Outline platelets.
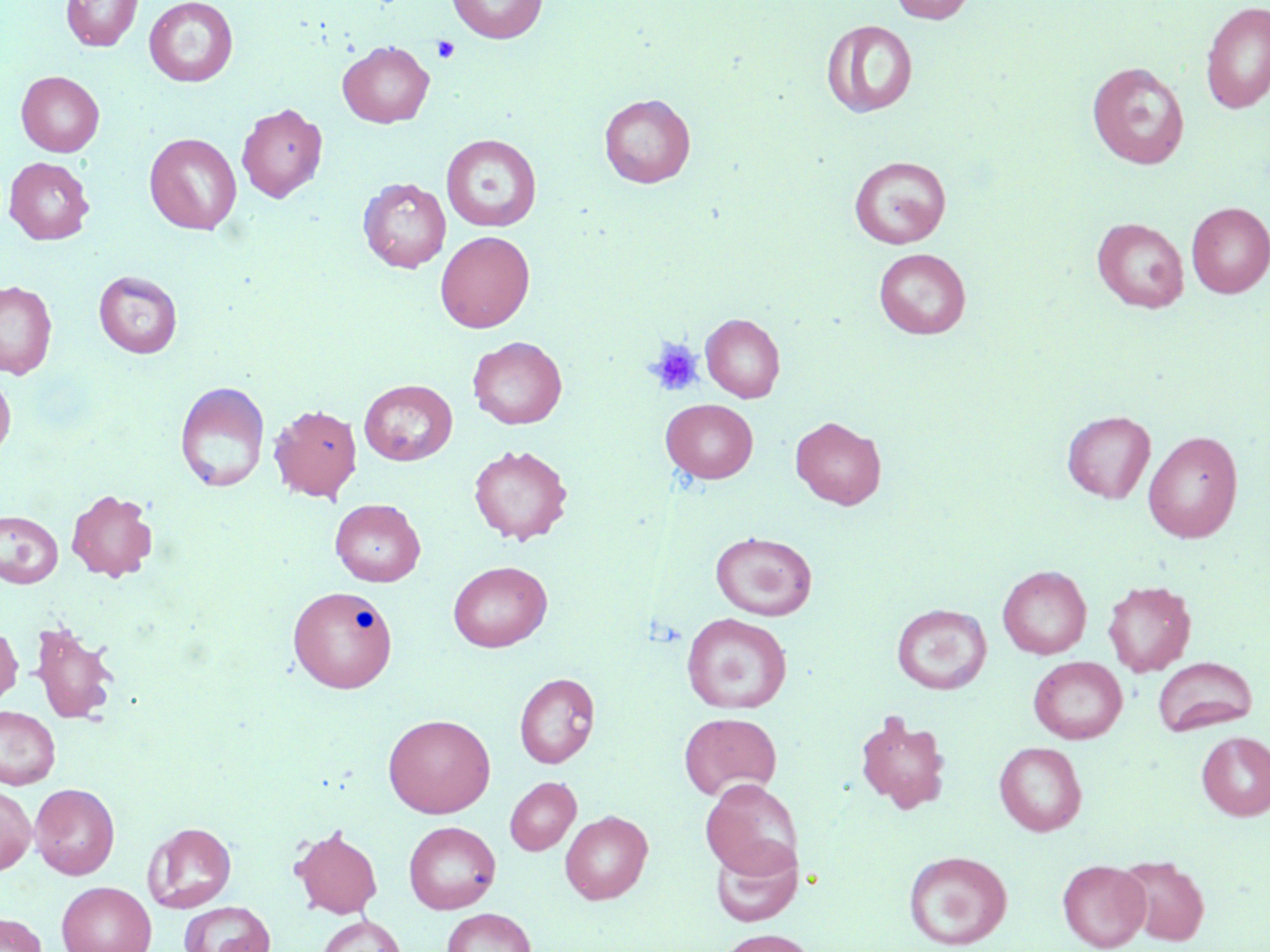

Approximate bounding boxes as named x1/y1/x2/y2 corners in pixels.
Platelets: (x1=432, y1=36, x2=460, y2=63), (x1=646, y1=338, x2=704, y2=396).

{
  "slide_level_diagnosis": "no evidence of blood parasites",
  "preparation": "thin blood film",
  "magnification": "1000x",
  "uninfected_red_blood_cell_locations": "approximate bounding boxes as named x1/y1/x2/y2 corners in pixels: (x1=60, y1=0, x2=143, y2=51), (x1=144, y1=0, x2=238, y2=87), (x1=446, y1=0, x2=547, y2=43), (x1=889, y1=0, x2=976, y2=24), (x1=1200, y1=2, x2=1270, y2=115), (x1=822, y1=20, x2=918, y2=118), (x1=338, y1=41, x2=434, y2=127), (x1=1087, y1=61, x2=1190, y2=169), (x1=16, y1=71, x2=104, y2=157), (x1=599, y1=94, x2=695, y2=188), (x1=237, y1=102, x2=327, y2=203), (x1=144, y1=132, x2=242, y2=234), (x1=441, y1=133, x2=542, y2=232), (x1=849, y1=156, x2=951, y2=249), (x1=4, y1=157, x2=94, y2=245), (x1=358, y1=177, x2=451, y2=273), (x1=1186, y1=202, x2=1270, y2=298), (x1=1092, y1=218, x2=1189, y2=313), (x1=435, y1=231, x2=534, y2=332), (x1=874, y1=248, x2=970, y2=339), (x1=94, y1=270, x2=183, y2=358), (x1=0, y1=280, x2=57, y2=379), (x1=701, y1=313, x2=785, y2=402), (x1=468, y1=336, x2=567, y2=429), (x1=0, y1=370, x2=15, y2=461), (x1=359, y1=379, x2=457, y2=466), (x1=175, y1=381, x2=270, y2=493), (x1=661, y1=399, x2=758, y2=483), (x1=269, y1=404, x2=362, y2=502), (x1=1062, y1=410, x2=1156, y2=503), (x1=791, y1=416, x2=886, y2=509), (x1=1143, y1=430, x2=1244, y2=543), (x1=469, y1=444, x2=573, y2=545), (x1=66, y1=489, x2=158, y2=581), (x1=330, y1=498, x2=425, y2=587), (x1=0, y1=511, x2=64, y2=588), (x1=711, y1=531, x2=817, y2=621), (x1=448, y1=561, x2=552, y2=652), (x1=998, y1=565, x2=1091, y2=659), (x1=1103, y1=580, x2=1196, y2=676), (x1=287, y1=586, x2=396, y2=692), (x1=891, y1=604, x2=992, y2=694), (x1=682, y1=613, x2=792, y2=714), (x1=29, y1=621, x2=120, y2=725), (x1=0, y1=623, x2=22, y2=707), (x1=1029, y1=656, x2=1127, y2=744), (x1=1153, y1=657, x2=1257, y2=736), (x1=514, y1=673, x2=600, y2=768), (x1=0, y1=706, x2=60, y2=789), (x1=853, y1=709, x2=952, y2=814), (x1=679, y1=712, x2=782, y2=800), (x1=383, y1=713, x2=495, y2=818), (x1=1197, y1=731, x2=1270, y2=820), (x1=994, y1=741, x2=1087, y2=836), (x1=505, y1=776, x2=581, y2=855), (x1=700, y1=778, x2=803, y2=879), (x1=29, y1=783, x2=120, y2=879), (x1=0, y1=785, x2=36, y2=874), (x1=560, y1=810, x2=653, y2=904), (x1=143, y1=821, x2=237, y2=913), (x1=404, y1=821, x2=501, y2=914), (x1=290, y1=825, x2=383, y2=919), (x1=710, y1=837, x2=803, y2=927), (x1=903, y1=850, x2=1011, y2=949), (x1=1116, y1=856, x2=1210, y2=946), (x1=1058, y1=860, x2=1150, y2=951), (x1=56, y1=881, x2=156, y2=952), (x1=178, y1=901, x2=275, y2=952), (x1=442, y1=907, x2=536, y2=952), (x1=0, y1=913, x2=46, y2=951), (x1=317, y1=915, x2=406, y2=952), (x1=717, y1=928, x2=816, y2=952)",
  "field_of_view": "single",
  "stain": "May-Grünwald-Giemsa",
  "modality": "optical microscopy",
  "image_size": "1270×952 pixels"
}